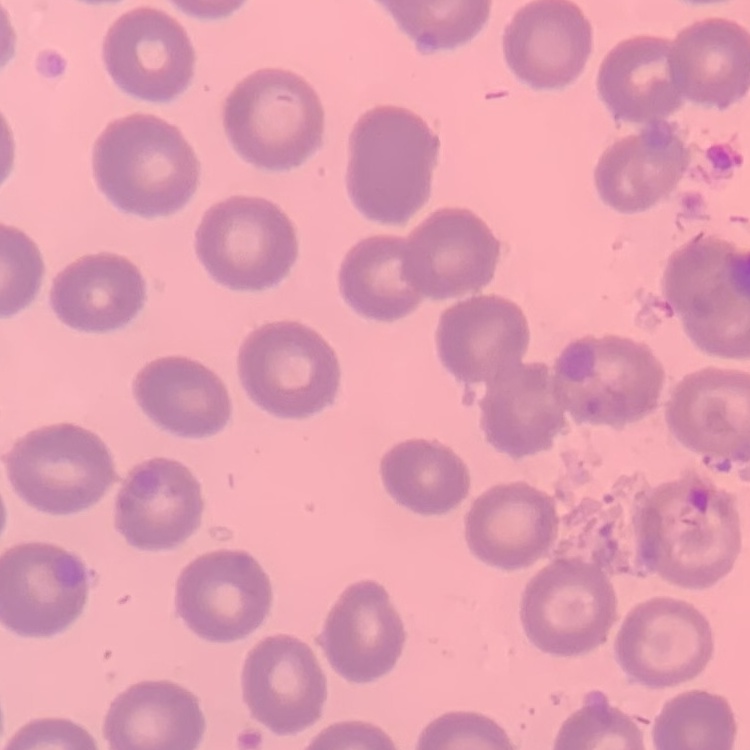

Summary:
  - Erythrocyte morphology: no rouleaux formation
  - Image type: one tile cut from a larger photomicrograph
  - Stain: Field's or Giemsa
  - Preparation: thin blood smear